Give the position of every Plasmodium parasite.
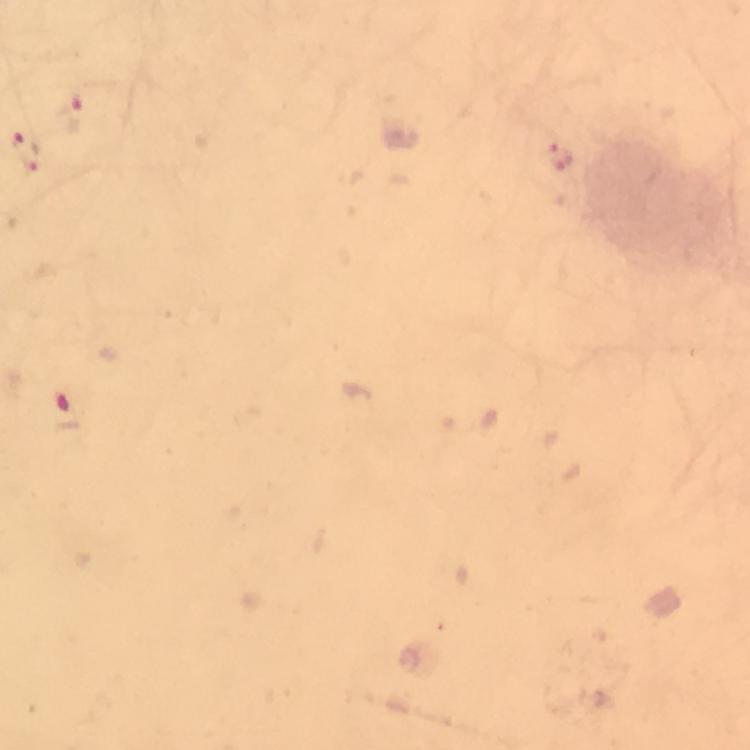
Approximate centers as (x, y) in pixels.
Plasmodium parasites: (72, 114), (28, 151), (559, 158), (69, 413).

preparation = thick blood film
cropped from = a single field of view
context = from a diagnostic examination for malaria
magnification = 100x
capture = smartphone photograph through a microscope
image size = 750×750 pixels
stain = Giemsa
immersion oil = applied